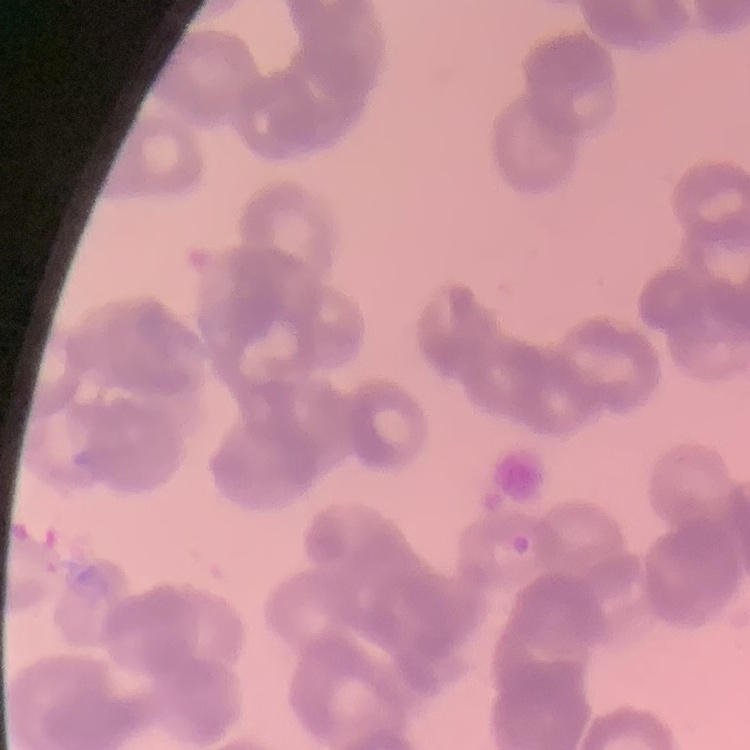
The erythrocytes show rouleaux formation. Thin blood smear. Square crop of a larger photomicrograph. Stained with either Field's or Giemsa.